Classify this cell by malaria status.
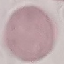
Uninfected.

Summary:
  - Stain: Giemsa
  - Capture: smartphone through the microscope eyepiece
  - Preparation: thin blood film
  - Image type: cell patch, automatically extracted from a larger field of view and resized to 64 × 64 pixels